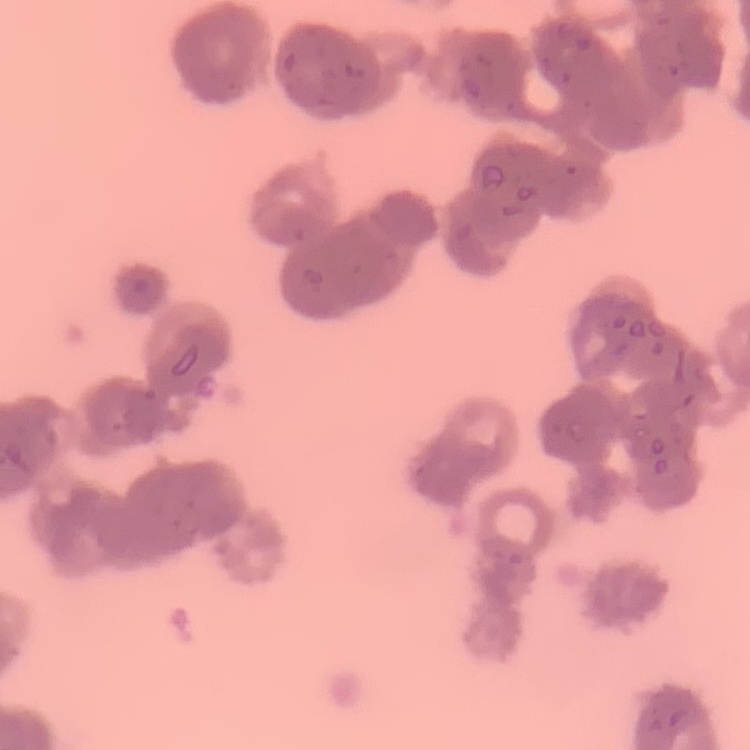
Summary:
  - Red blood cell morphology: rouleaux formation
  - Stain: Field's or Giemsa
  - Preparation: thin peripheral smear
  - Image type: square crop of a larger photomicrograph